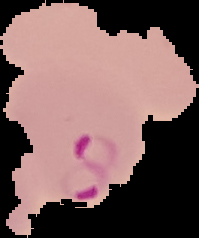
From a thin blood smear. Cell region segmented out of the field of view; the surrounding area is masked to black. Image is 199×238 pixels. Malaria status: parasitized.